State which parasite is depicted.
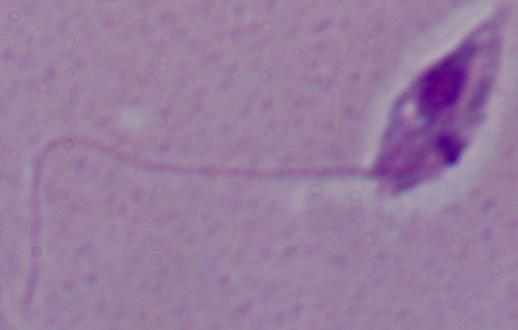
This is Leishmania.

1000x magnification. Micrograph.